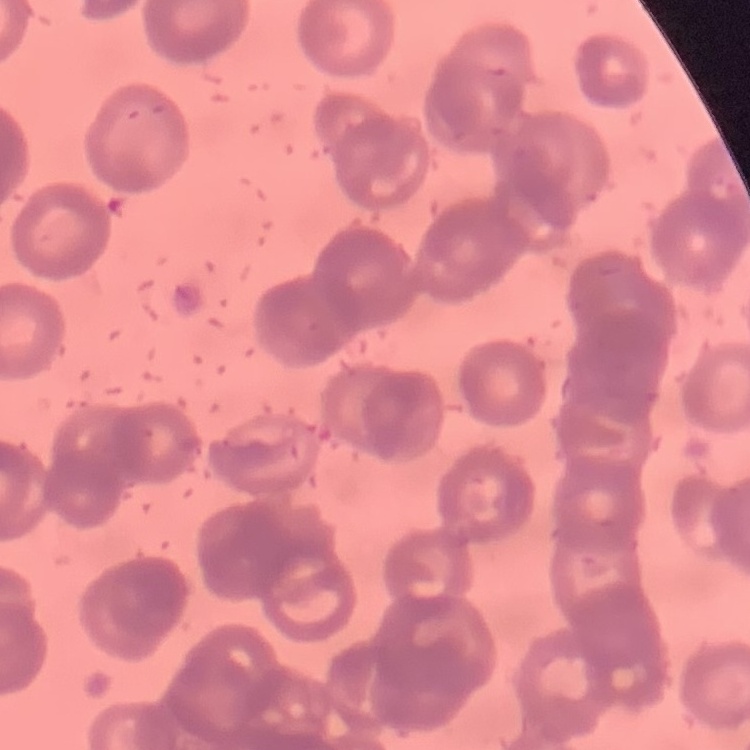

Summary:
  - Red blood cell morphology: rouleaux formation
  - Stain: Field's or Giemsa
  - Image type: square crop of a larger photomicrograph
  - Preparation: thin blood smear